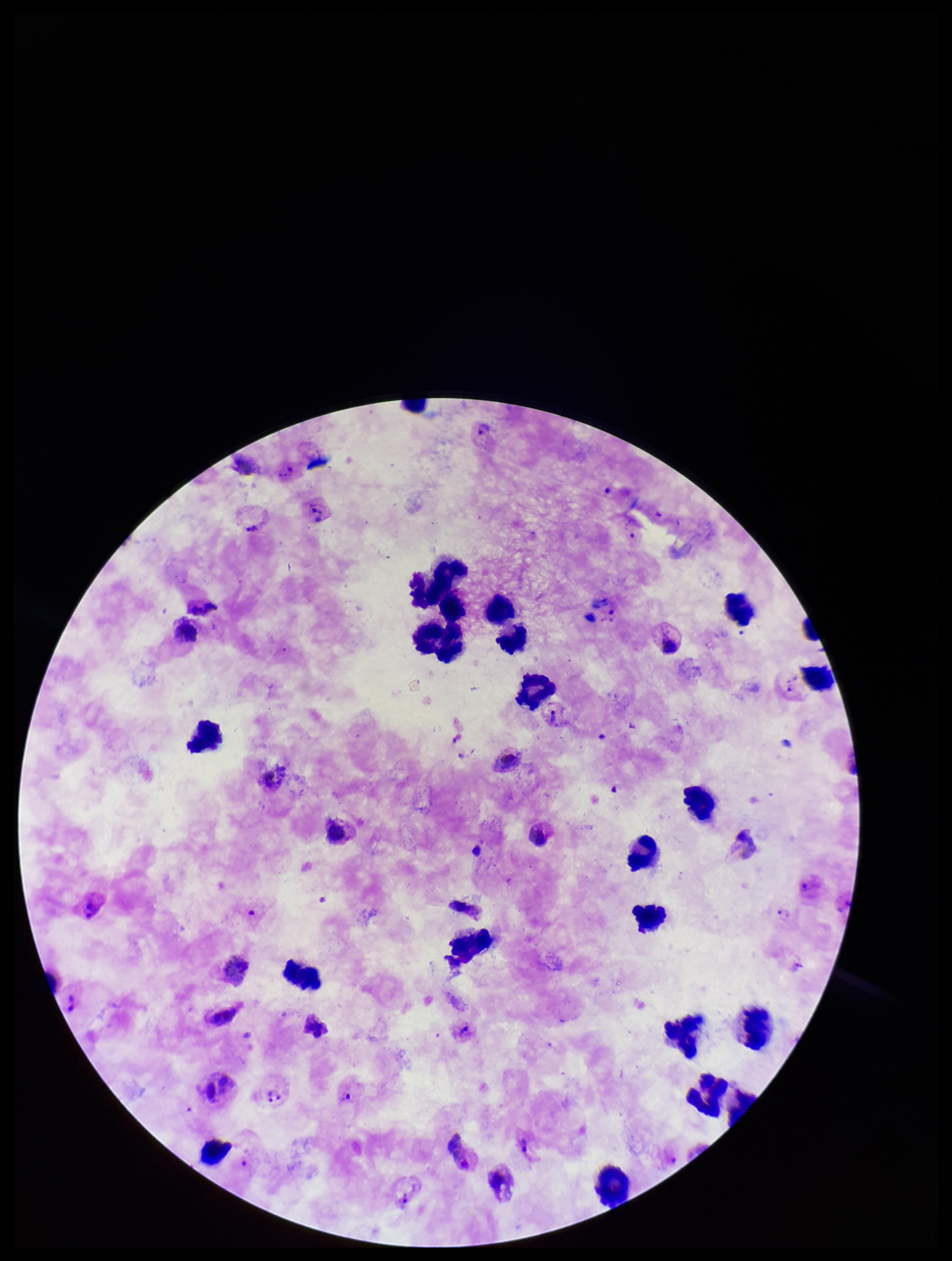

stain: Giemsa
leukocyte_count: 26
capture: smartphone photograph through the microscope eyepiece
field_of_view: single
patient_malaria_status: positive
preparation: thick
plasmodium_parasites: detected
image_size: 952×1261 pixels
parasite_count: 10
species_reported_for_this_patient: Plasmodium vivax